Name the parasite shown.
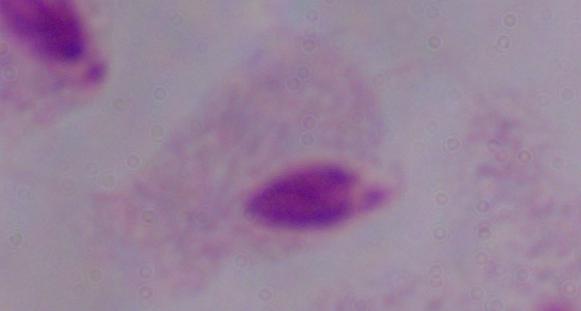

A trichomonad.

{
  "magnification": "1000x",
  "modality": "micrograph"
}